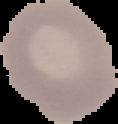
Summary:
  - Malaria status: uninfected
  - Preparation: thin blood smear
  - Image type: segmented cell region on a black background
  - Image size: 118×124 pixels